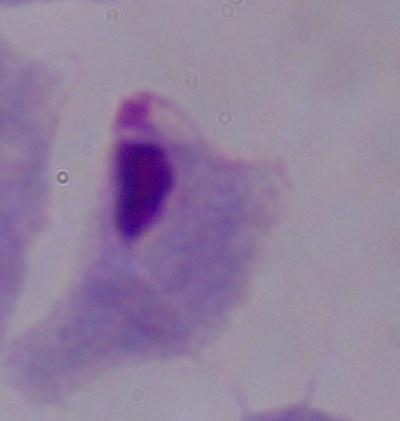

{
  "modality": "micrograph",
  "magnification": "1000x",
  "identification": "trichomonad"
}